Classify this cell by malaria status.
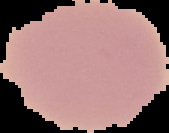

Uninfected.

image size = 169×133 pixels
preparation = thin blood smear
image type = cell region segmented out of the field of view; surrounding area masked to black